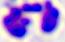

modality: photomicrograph
magnification: 400x
identification: white blood cell